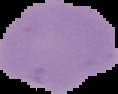

{
  "image_type": "segmented cell region with the area outside set to black",
  "preparation": "thin blood film",
  "result": "negative for Plasmodium parasites",
  "image_size": "118×94 pixels"
}